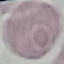

malaria_status: uninfected
capture: smartphone through the microscope eyepiece
preparation: thin blood film
image_type: automatically extracted cell patch, resized to 64 × 64 pixels
stain: Giemsa